Report the malaria status of this cell.
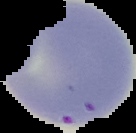

Parasitized.

preparation = thin blood film
image size = 136×133 pixels
image type = segmented cell region on a black background